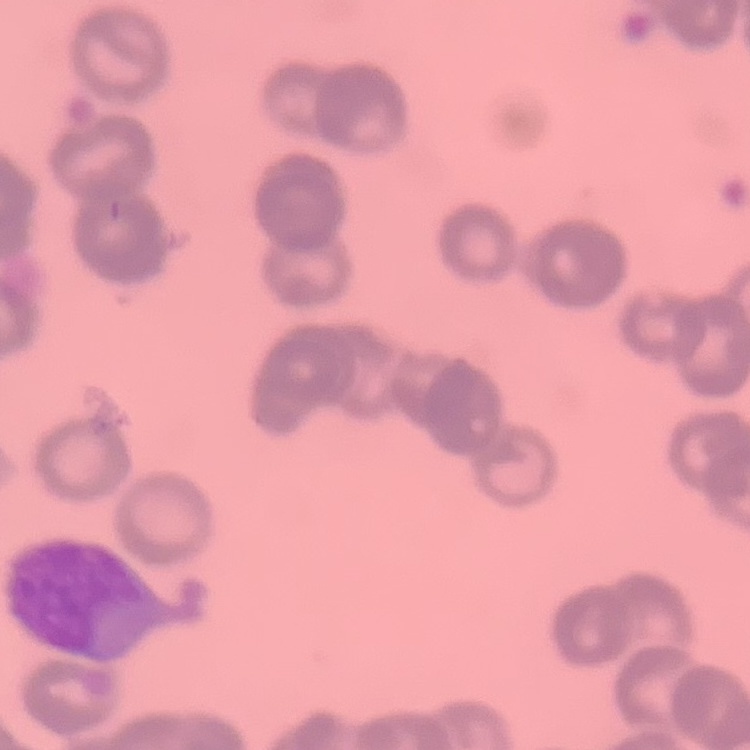 The erythrocytes exhibit rouleaux formation. Square crop of a larger photomicrograph. Thin blood smear. Field's or Giemsa stain.